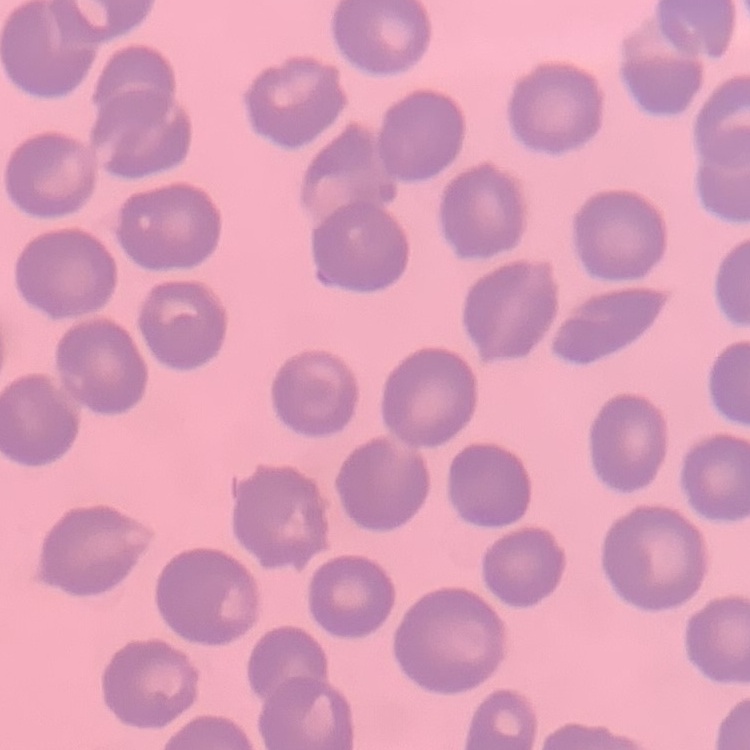 The red blood cells exhibit no rouleaux formation. Thin peripheral smear. Field's or Giemsa stain. One tile cut from a larger photomicrograph.